Name the parasite shown.
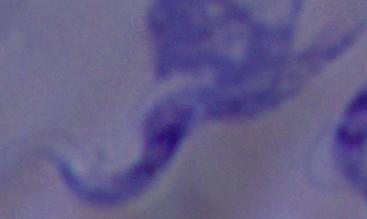
This is a trypanosome.

Summary:
  - Magnification: 1000x
  - Modality: photomicrograph